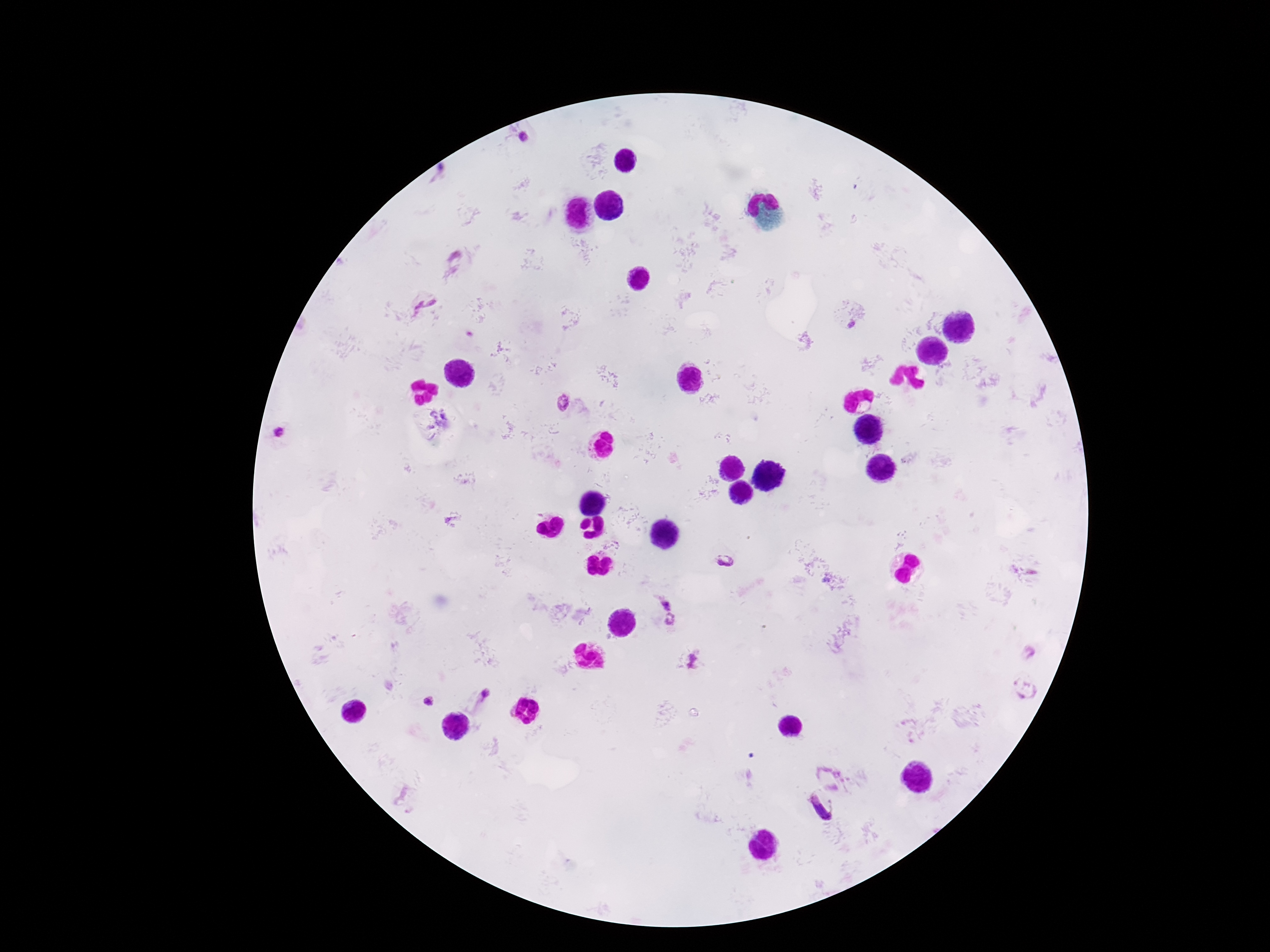
Approximate centers as [x, y] in pixels.
Summary:
  - Plasmodium parasite locations: [523, 139], [427, 304], [852, 325], [563, 404], [279, 433], [723, 559], [666, 604], [670, 619], [692, 660], [1024, 688], [487, 696], [427, 702], [829, 776], [823, 808]
  - Magnification: 100x
  - Stain: Giemsa
  - Capture: smartphone camera through the microscope eyepiece
  - Preparation: thick blood smear
  - Image size: 1270×952 pixels
  - Patient malaria status: positive
  - Field of view: single